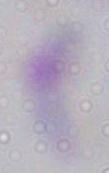

Summary:
  - Modality: micrograph
  - Magnification: 1000x
  - Identification: Toxoplasma gondii